Assess the morphology of the red blood cells.
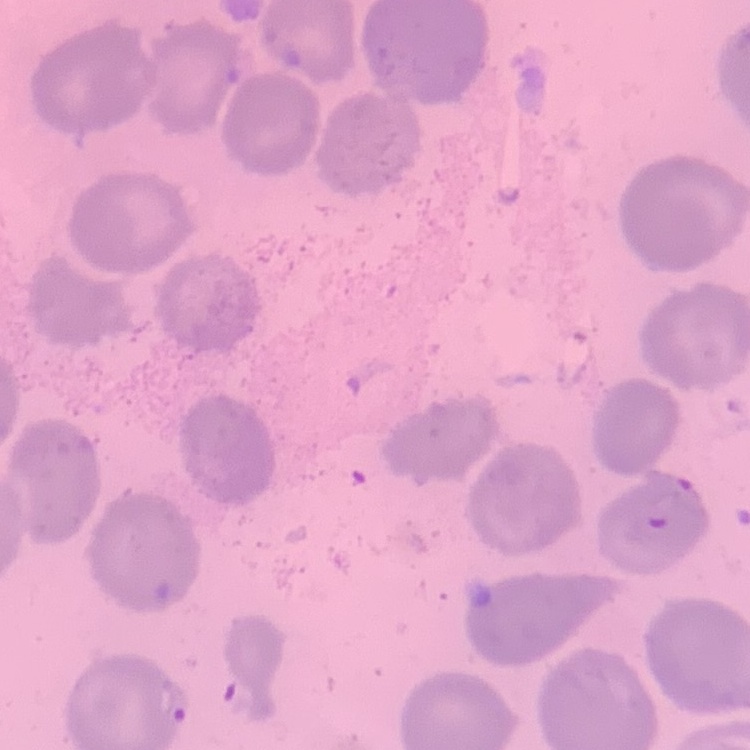
They show no rouleaux formation.

image type = square crop of a larger photomicrograph
stain = Field's or Giemsa
preparation = thin blood smear